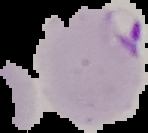
From a thin blood smear. Cell region segmented out of the field of view; the surrounding area is masked to black. Malaria status: parasitized. Image is 148×133 pixels.